Locate every blood parasite and identify its species.
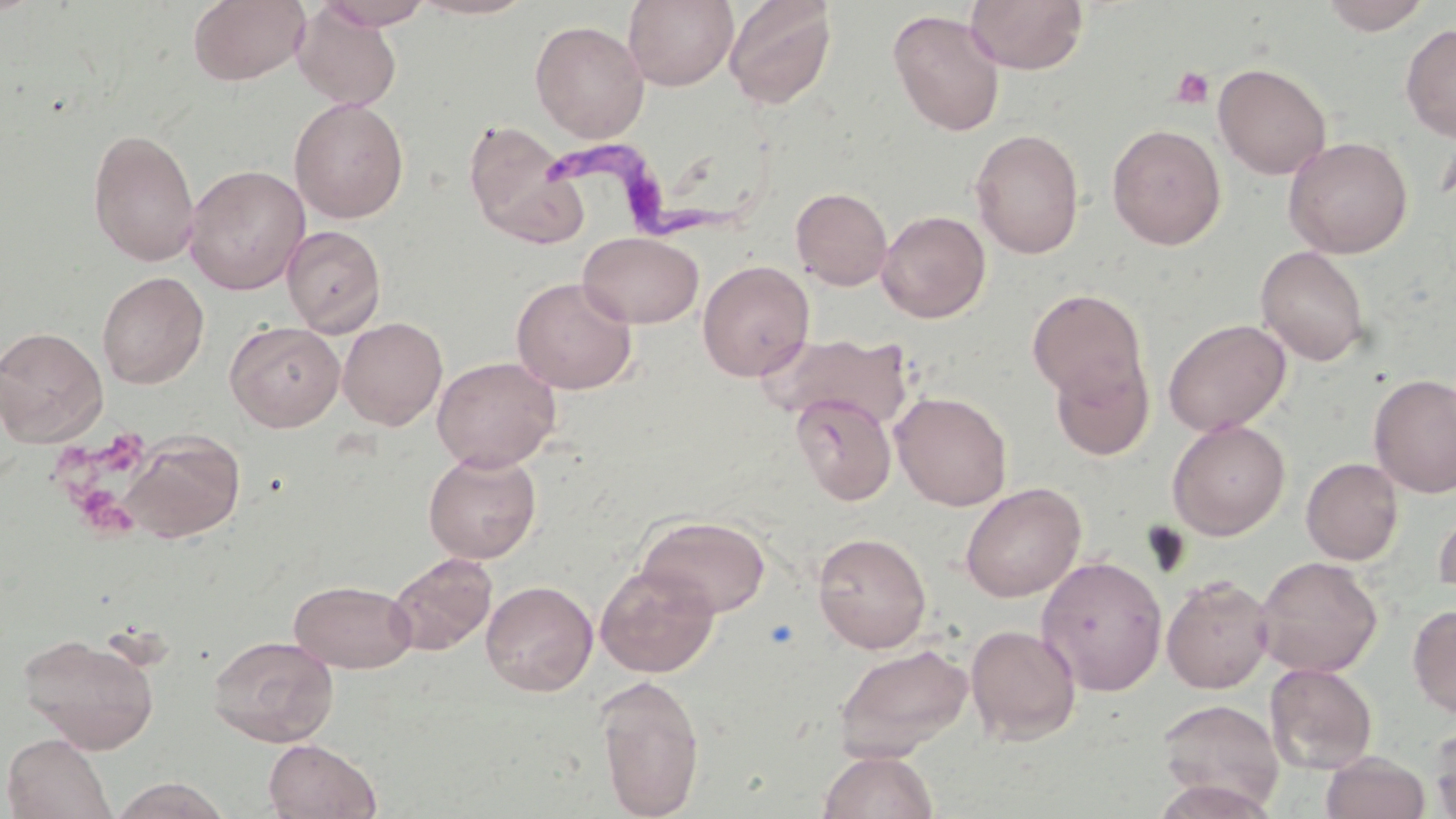

Approximate bounding boxes as [x1, y1, x2, y2] in pixels.
Trypanosoma brucei: [546, 135, 748, 242].
No Plasmodium falciparum, Plasmodium ovale, Plasmodium malariae, Plasmodium vivax, or Babesia divergens observed.

Summary:
  - Uninfected red blood cell locations: [188, 0, 310, 86], [409, 0, 539, 20], [623, 0, 738, 90], [723, 0, 838, 109], [965, 0, 1089, 74], [1319, 0, 1433, 35], [316, 1, 436, 29], [292, 4, 402, 110], [888, 9, 1006, 137], [530, 20, 649, 141], [1400, 23, 1456, 141], [1213, 62, 1331, 180], [289, 97, 410, 224], [463, 119, 586, 247], [1107, 123, 1226, 250], [87, 127, 200, 267], [970, 128, 1085, 259], [1283, 136, 1413, 258], [184, 164, 310, 294], [791, 186, 893, 290], [876, 210, 991, 323], [281, 225, 386, 336], [577, 231, 704, 328], [1255, 245, 1371, 366], [697, 260, 814, 381], [96, 272, 208, 389], [511, 276, 638, 394], [1026, 288, 1149, 403], [337, 317, 447, 430], [1162, 318, 1292, 436], [225, 320, 345, 432], [0, 326, 108, 446], [760, 331, 914, 430], [1049, 351, 1154, 462], [431, 356, 561, 472], [1368, 372, 1456, 498], [892, 391, 1012, 510], [790, 392, 897, 506], [1167, 419, 1290, 540], [120, 431, 245, 543], [423, 449, 543, 564], [1301, 457, 1404, 565], [960, 482, 1086, 602], [1432, 500, 1456, 604], [637, 515, 772, 618], [811, 531, 932, 653], [387, 552, 497, 656], [1036, 554, 1168, 696], [1254, 555, 1383, 677], [595, 563, 720, 678], [1161, 575, 1273, 693], [289, 579, 417, 673], [480, 580, 598, 696], [1408, 604, 1456, 719], [965, 623, 1082, 745], [17, 631, 161, 752], [207, 634, 339, 746], [833, 642, 974, 760], [1264, 662, 1378, 774], [593, 675, 705, 819], [1156, 698, 1285, 813], [1427, 721, 1456, 819], [2, 733, 116, 818], [263, 738, 382, 819], [817, 750, 939, 819], [1320, 751, 1431, 819], [108, 776, 233, 819]
  - Platelet locations: [1169, 66, 1215, 109], [49, 426, 159, 540], [762, 618, 801, 651]
  - Slide-level diagnosis: Trypanosoma brucei
  - Preparation: thin blood smear
  - Field of view: one of a larger specimen
  - Magnification: 1000x
  - Stain: May-Grünwald-Giemsa
  - Image size: 1456×819 pixels
  - Modality: optical microscopy